Classify this cell by malaria status.
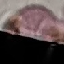

It is uninfected.

Summary:
  - Preparation: thin blood film
  - Capture: smartphone through the microscope eyepiece
  - Stain: Giemsa
  - Image type: automatically extracted cell patch, resized to 64 × 64 pixels